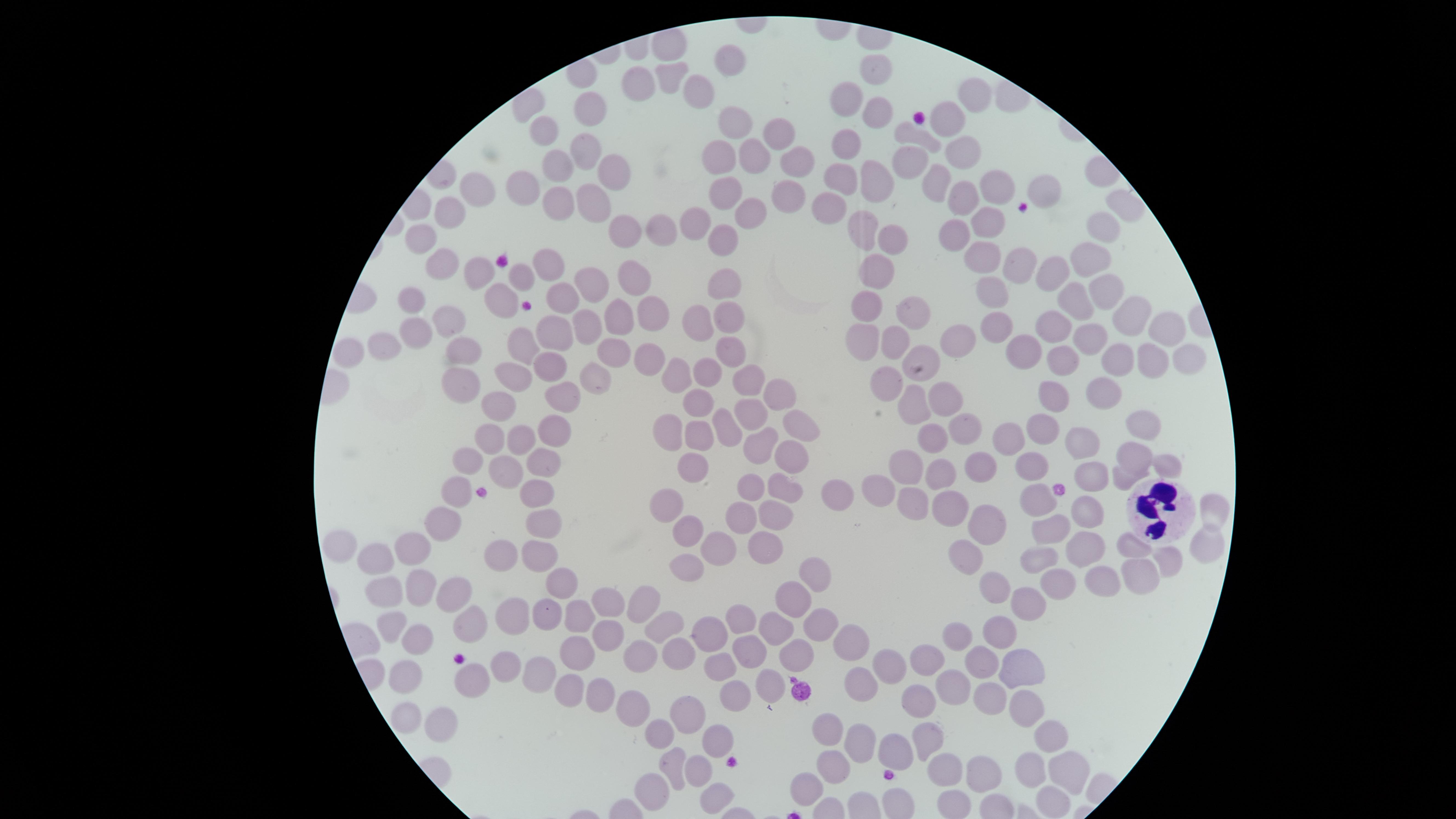 Approximate marker points, in pixels from the top-left corner. White blood cells: (x=1155, y=510). Uninfected red blood cells: (x=663, y=42), (x=735, y=59), (x=875, y=67), (x=665, y=75), (x=635, y=82), (x=699, y=88), (x=976, y=95), (x=847, y=99), (x=589, y=103), (x=876, y=116), (x=948, y=116), (x=735, y=118), (x=541, y=131), (x=774, y=134), (x=919, y=136), (x=849, y=145), (x=580, y=151), (x=719, y=152), (x=961, y=152), (x=912, y=156), (x=751, y=157), (x=556, y=160), (x=794, y=161), (x=601, y=165), (x=839, y=174), (x=933, y=180), (x=875, y=181), (x=993, y=185), (x=525, y=187), (x=1042, y=190), (x=726, y=191), (x=478, y=193), (x=960, y=196), (x=784, y=199), (x=591, y=200), (x=557, y=203), (x=1122, y=203), (x=831, y=204), (x=749, y=212), (x=447, y=213), (x=988, y=220), (x=694, y=221), (x=1105, y=223), (x=615, y=228), (x=864, y=228), (x=652, y=233), (x=958, y=233), (x=422, y=237), (x=723, y=239), (x=889, y=239), (x=1090, y=253), (x=991, y=255), (x=439, y=261), (x=1019, y=261), (x=550, y=266), (x=874, y=269), (x=1060, y=269), (x=474, y=275), (x=519, y=275), (x=631, y=279), (x=593, y=288), (x=723, y=289), (x=995, y=289), (x=1105, y=289), (x=499, y=297), (x=1077, y=298), (x=558, y=299), (x=407, y=300), (x=868, y=304), (x=657, y=313), (x=910, y=313), (x=1129, y=313), (x=452, y=314), (x=728, y=317), (x=621, y=321), (x=989, y=322), (x=592, y=323), (x=700, y=323), (x=1055, y=324), (x=1160, y=325), (x=552, y=333), (x=418, y=334), (x=1087, y=334), (x=960, y=338), (x=523, y=341), (x=864, y=341), (x=382, y=345), (x=893, y=345), (x=461, y=347), (x=352, y=349), (x=732, y=349), (x=1019, y=349), (x=613, y=352), (x=645, y=358), (x=1118, y=358), (x=1149, y=359), (x=1066, y=360), (x=925, y=362), (x=1182, y=362), (x=547, y=365), (x=514, y=370), (x=707, y=371), (x=678, y=373), (x=598, y=378), (x=889, y=378), (x=750, y=379), (x=460, y=383), (x=1101, y=388), (x=948, y=395), (x=1059, y=395), (x=564, y=396), (x=777, y=398), (x=695, y=401), (x=499, y=402), (x=918, y=407), (x=752, y=413), (x=801, y=420), (x=726, y=422), (x=1142, y=422), (x=967, y=424), (x=673, y=425), (x=1041, y=425), (x=552, y=428), (x=481, y=432), (x=696, y=434), (x=521, y=436), (x=1085, y=438), (x=757, y=441), (x=933, y=441), (x=1009, y=441), (x=1131, y=455), (x=792, y=456), (x=469, y=459), (x=544, y=459), (x=977, y=460), (x=908, y=463), (x=1029, y=463), (x=1169, y=466), (x=507, y=468), (x=693, y=470), (x=941, y=475), (x=1091, y=475), (x=1120, y=479), (x=878, y=485), (x=745, y=487), (x=786, y=487), (x=456, y=488), (x=535, y=489), (x=663, y=499), (x=835, y=499), (x=1038, y=499), (x=919, y=502), (x=953, y=505), (x=1210, y=507), (x=1088, y=509), (x=771, y=516), (x=740, y=517), (x=546, y=522), (x=443, y=525), (x=994, y=525), (x=685, y=531), (x=1041, y=535), (x=715, y=543), (x=410, y=547), (x=1086, y=547), (x=1203, y=547), (x=757, y=548), (x=1137, y=548), (x=345, y=551), (x=500, y=554), (x=539, y=554), (x=971, y=555), (x=375, y=560), (x=1170, y=561), (x=1035, y=564), (x=684, y=569), (x=813, y=575), (x=1139, y=576), (x=1097, y=581), (x=560, y=584), (x=1053, y=585), (x=415, y=586), (x=994, y=590), (x=379, y=596), (x=447, y=596), (x=643, y=601), (x=793, y=601), (x=1027, y=604), (x=609, y=606), (x=548, y=610), (x=516, y=614), (x=578, y=617), (x=742, y=618), (x=395, y=624), (x=470, y=625), (x=663, y=625), (x=819, y=628), (x=774, y=630), (x=712, y=633), (x=1000, y=633), (x=605, y=636), (x=960, y=636), (x=416, y=640), (x=851, y=642), (x=577, y=648), (x=677, y=653), (x=644, y=655), (x=750, y=655), (x=802, y=657), (x=927, y=661), (x=982, y=661), (x=503, y=663), (x=888, y=663), (x=1016, y=664), (x=721, y=665), (x=538, y=669), (x=408, y=673), (x=469, y=682), (x=952, y=682), (x=770, y=684), (x=858, y=684), (x=569, y=689), (x=592, y=690), (x=732, y=693), (x=988, y=697), (x=915, y=701), (x=1024, y=706), (x=634, y=708), (x=685, y=711), (x=408, y=713), (x=439, y=720), (x=828, y=728), (x=1046, y=734), (x=660, y=735), (x=724, y=735), (x=923, y=737), (x=859, y=738), (x=892, y=748), (x=1073, y=764), (x=673, y=765), (x=834, y=766), (x=701, y=769), (x=1031, y=770), (x=951, y=773), (x=982, y=774), (x=808, y=786), (x=654, y=790), (x=713, y=798), (x=1052, y=798). Giemsa-stained preparation. One field of view of the specimen. Image is 1456×819 pixels. Presence: no malaria parasites detected. Thin blood smear. Smartphone photograph through the microscope eyepiece. Circular visible region.